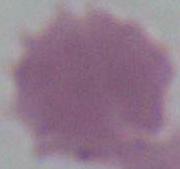
Photomicrograph. A red blood cell is seen. 1000x magnification.